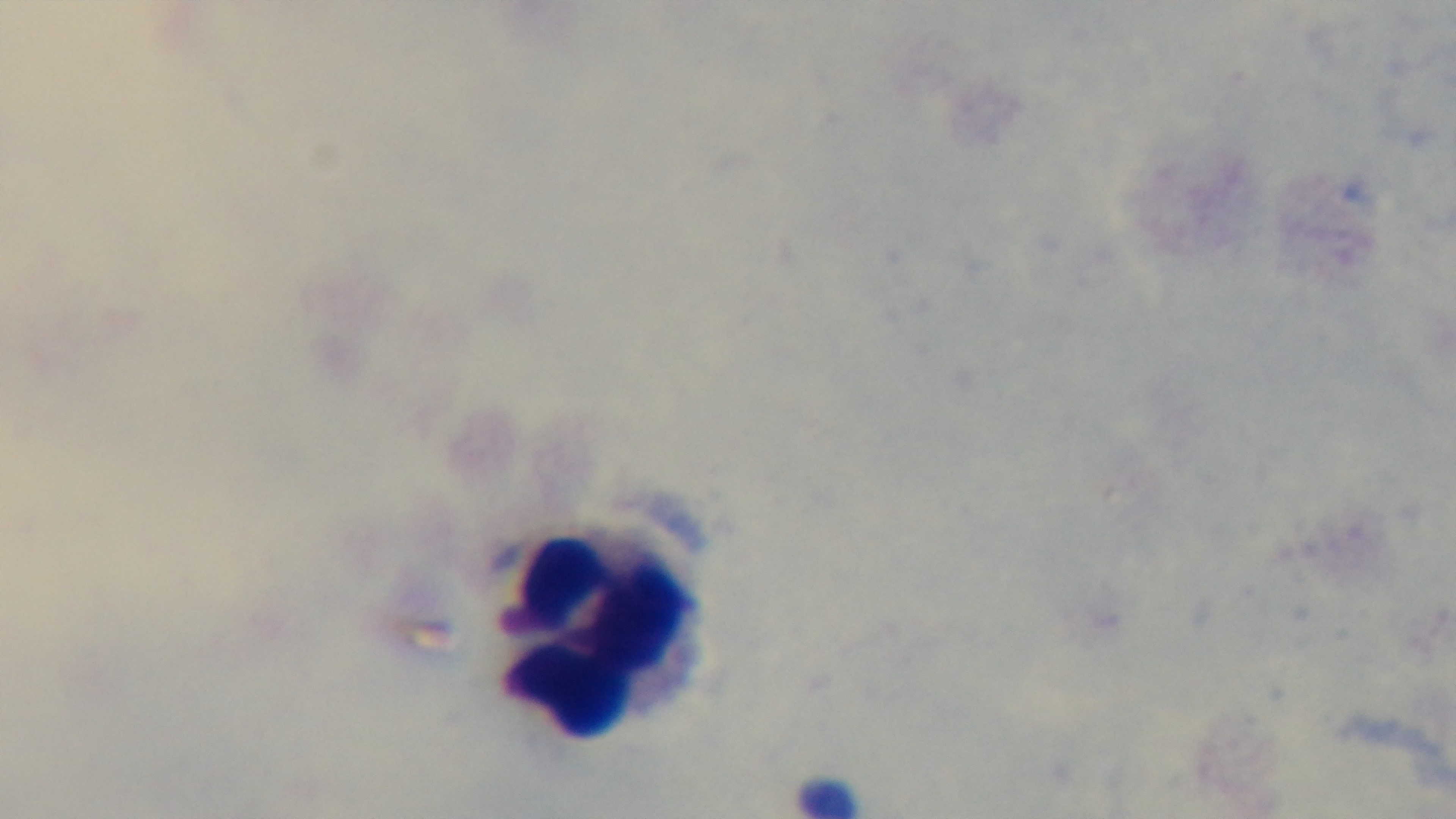
preparation: thick smear
capture: mounted 4K digital camera
objective: 100x oil immersion
modality: light microscopy
field_of_view: one from the slide
malaria_status: uninfected
stain: Giemsa